Assess this cell for malaria.
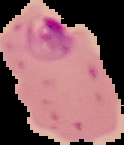

Parasitized.

Summary:
  - Preparation: thin blood film
  - Image type: cell region segmented out of the field of view; surrounding area masked to black
  - Image size: 124×145 pixels